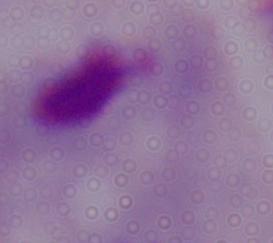

identification = trichomonad
modality = micrograph
magnification = 1000x